Give the position of every Plasmodium parasite.
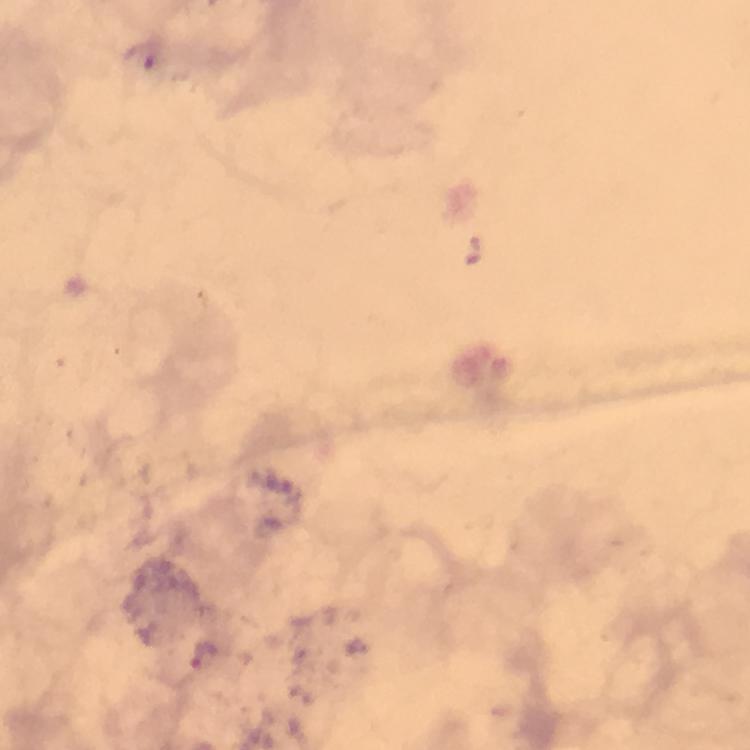
Approximate object centers, in pixels from the top-left corner.
Plasmodium parasites: (x=200, y=655).

{
  "stain": "Giemsa",
  "context": "from a diagnostic examination for malaria",
  "magnification": "100x",
  "image_size": "750×750 pixels",
  "preparation": "thick blood film",
  "immersion_oil": "used",
  "capture": "smartphone photograph through a microscope",
  "cropped_from": "one field of view"
}